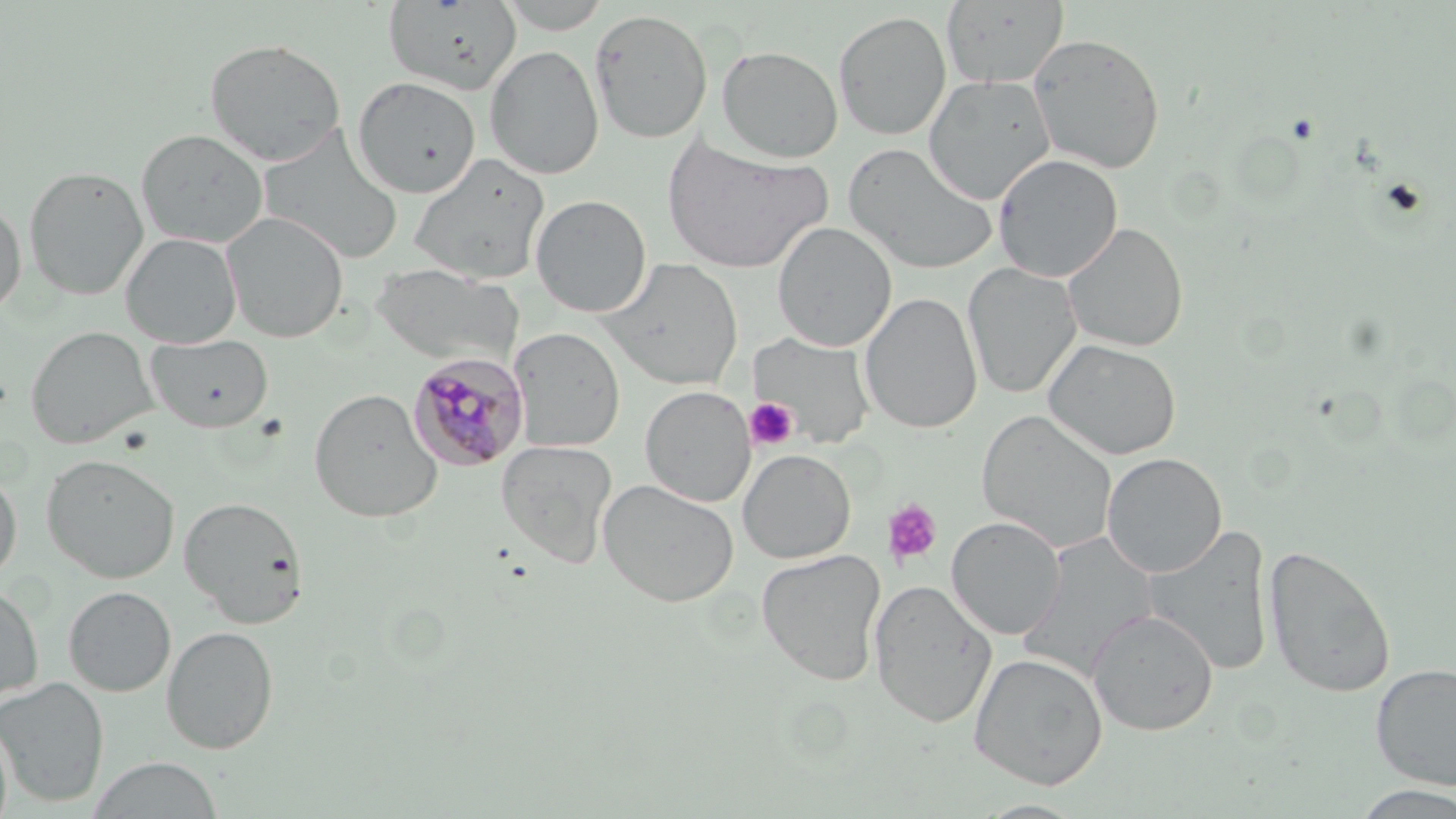

Approximate bounding boxes as [x1, y1, x2, y2] in pixels. Plasmodium malariae-infected red blood cell locations: [407, 352, 530, 472]. Platelet locations: [745, 396, 800, 450], [881, 498, 944, 569]. Uninfected red blood cell locations: [384, 0, 521, 94], [497, 0, 614, 34], [941, 0, 1070, 88], [590, 8, 713, 144], [833, 10, 952, 141], [1027, 32, 1166, 174], [204, 38, 347, 166], [485, 45, 604, 179], [716, 45, 843, 162], [923, 74, 1055, 204], [352, 76, 480, 198], [136, 128, 268, 247], [259, 130, 404, 264], [661, 134, 833, 274], [844, 142, 998, 274], [409, 153, 550, 284], [993, 153, 1123, 282], [23, 165, 148, 301], [531, 194, 651, 317], [0, 201, 27, 319], [222, 213, 348, 343], [772, 222, 896, 352], [1063, 222, 1188, 353], [121, 232, 242, 348], [600, 258, 744, 391], [371, 263, 522, 367], [963, 263, 1082, 399], [860, 292, 983, 434], [25, 325, 157, 448], [510, 327, 625, 452], [145, 333, 274, 433], [748, 333, 877, 450], [1043, 338, 1182, 461], [640, 385, 755, 507], [308, 388, 442, 523], [976, 410, 1119, 553], [496, 439, 617, 567], [738, 449, 856, 563], [1102, 452, 1226, 578], [42, 453, 180, 584], [0, 468, 22, 583], [598, 479, 739, 607], [179, 495, 309, 628], [946, 516, 1066, 640], [1144, 525, 1275, 676], [1017, 532, 1160, 681], [1263, 543, 1397, 698], [757, 549, 886, 686], [869, 579, 997, 728], [0, 582, 44, 703], [64, 586, 176, 696], [1087, 610, 1219, 736], [161, 625, 279, 754], [969, 652, 1108, 790], [1371, 662, 1456, 790], [0, 676, 109, 809], [87, 756, 224, 818], [1349, 785, 1456, 818], [974, 799, 1088, 818]. Slide-level diagnosis: Plasmodium malariae. Thin blood smear. Image is 1456×819 pixels. Light microscopy. May-Grünwald-Giemsa stain. Single field of view. 1000x magnification.